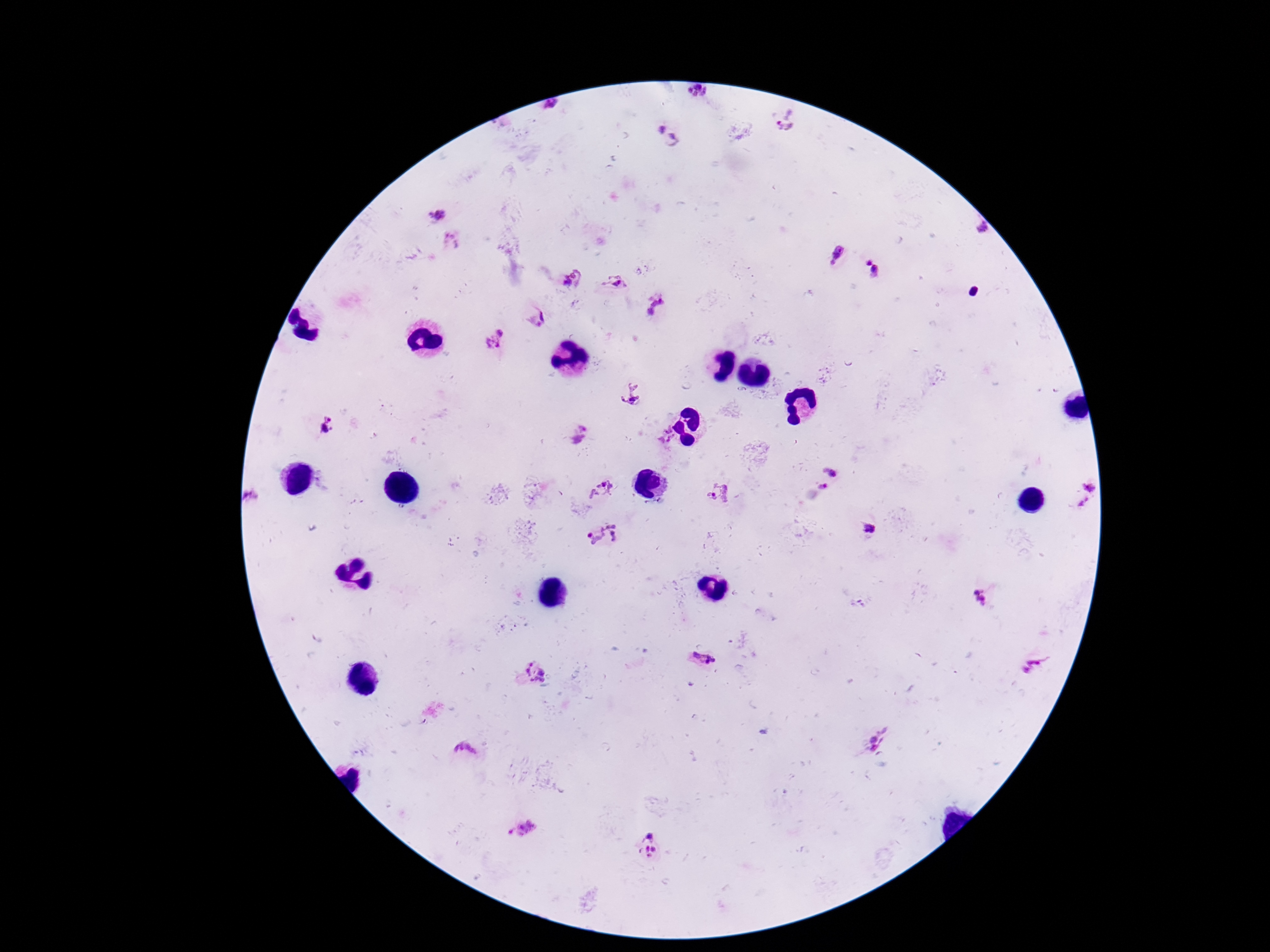
Approximate object centers, in pixels from the top-left corner.
Summary:
  - Plasmodium parasite locations: (x=696, y=91), (x=551, y=105), (x=786, y=120), (x=658, y=128), (x=677, y=140), (x=437, y=216), (x=983, y=228), (x=451, y=241), (x=837, y=254), (x=868, y=262), (x=877, y=272), (x=572, y=279), (x=615, y=281), (x=657, y=304), (x=538, y=319), (x=495, y=339), (x=632, y=396), (x=327, y=424), (x=665, y=434), (x=579, y=435), (x=832, y=471), (x=1090, y=484), (x=823, y=486), (x=602, y=489), (x=719, y=492), (x=251, y=496), (x=1084, y=502), (x=872, y=531), (x=605, y=535), (x=981, y=598), (x=703, y=661), (x=1035, y=665), (x=537, y=673), (x=878, y=739), (x=465, y=751), (x=523, y=826), (x=651, y=836), (x=649, y=851)
  - Patient malaria status: positive
  - Magnification: 100x
  - Image size: 1270×952 pixels
  - Preparation: thick blood smear
  - Stain: Giemsa
  - Field of view: single
  - Capture: smartphone camera through the microscope eyepiece